Identify the cell.
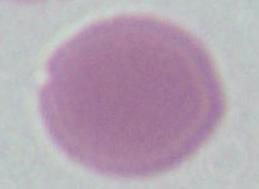

This is an erythrocyte.

magnification = 1000x
modality = photomicrograph